Give the preparation type.
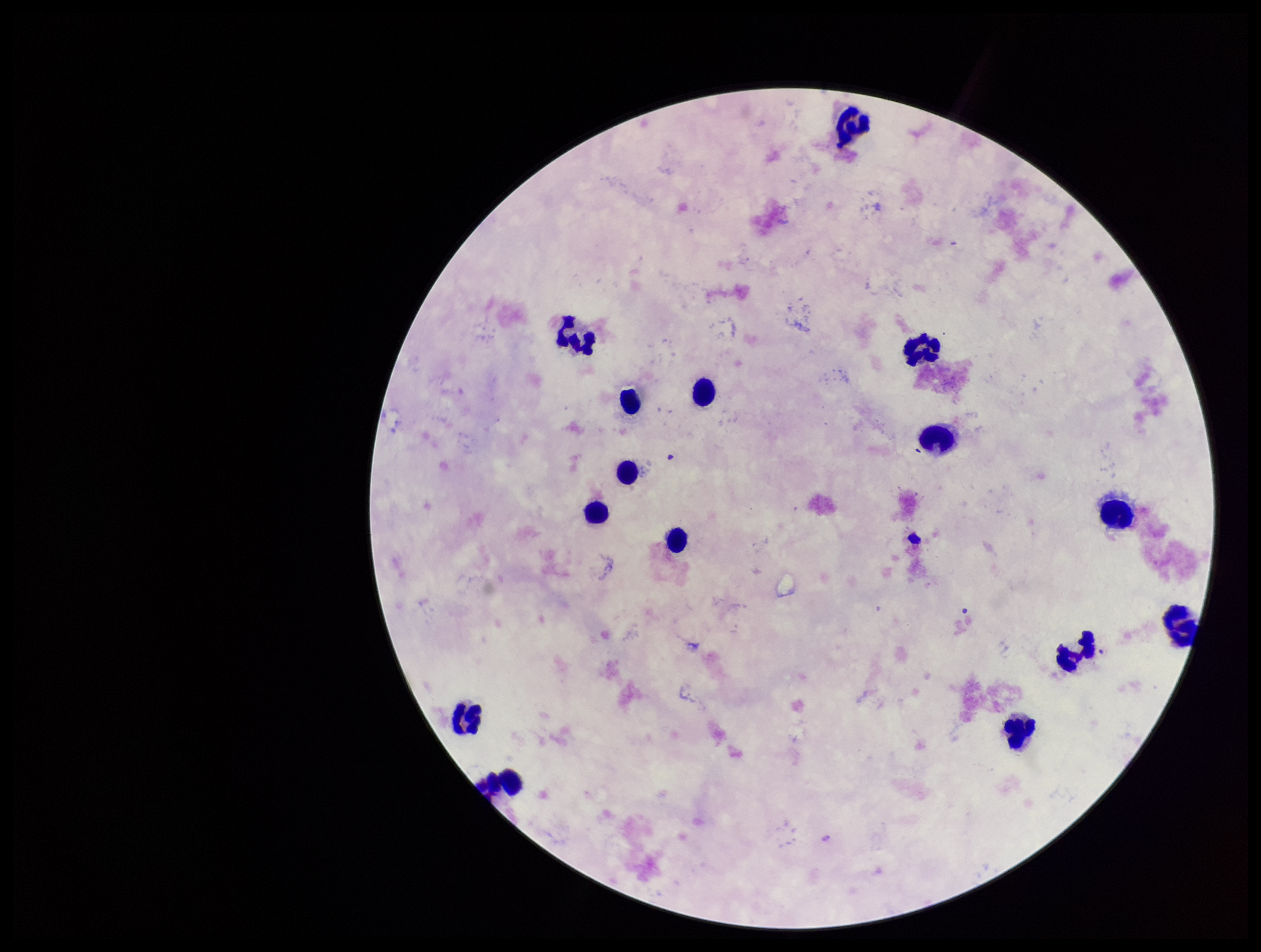
A thick smear.

{
  "leukocyte_count": 16,
  "stain": "Giemsa",
  "field_of_view": "one from this slide",
  "plasmodium_parasites": "none detected",
  "parasite_count": 0,
  "patient_malaria_status": "negative",
  "capture": "smartphone photograph through the microscope eyepiece",
  "image_size": "1261×952 pixels"
}